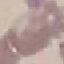
Summary:
  - Malaria status: uninfected
  - Capture: smartphone through the microscope eyepiece
  - Stain: Giemsa
  - Image type: automatically extracted cell patch, resized to 64 × 64 pixels
  - Preparation: thin smear